Give the preparation type.
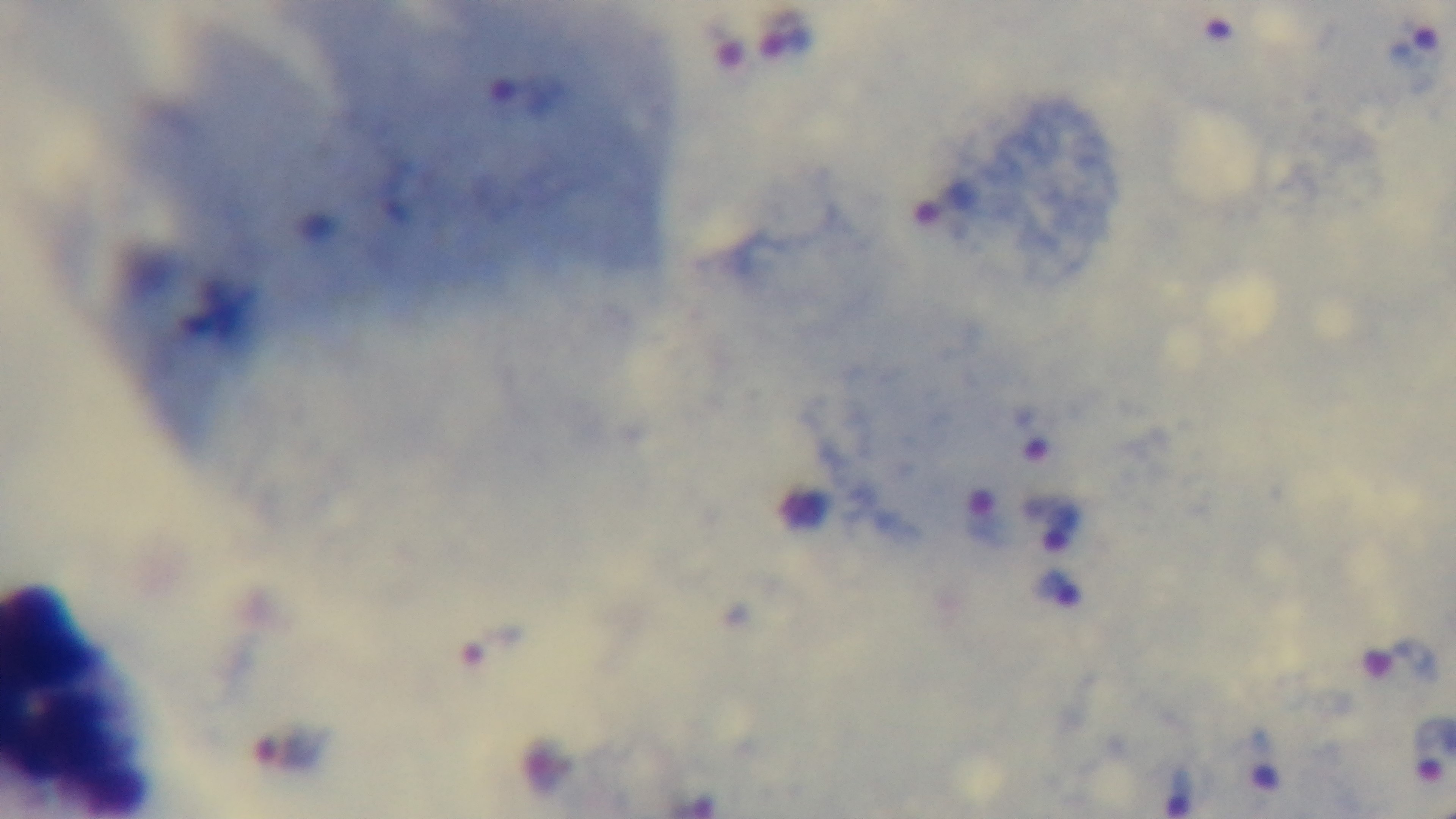

It is a thick blood film.

capture = mounted 4K digital camera
field of view = one from the slide
modality = light microscopy
stain = Giemsa
objective = 100x oil immersion
malaria status = infected